Locate every blood parasite and identify its species.
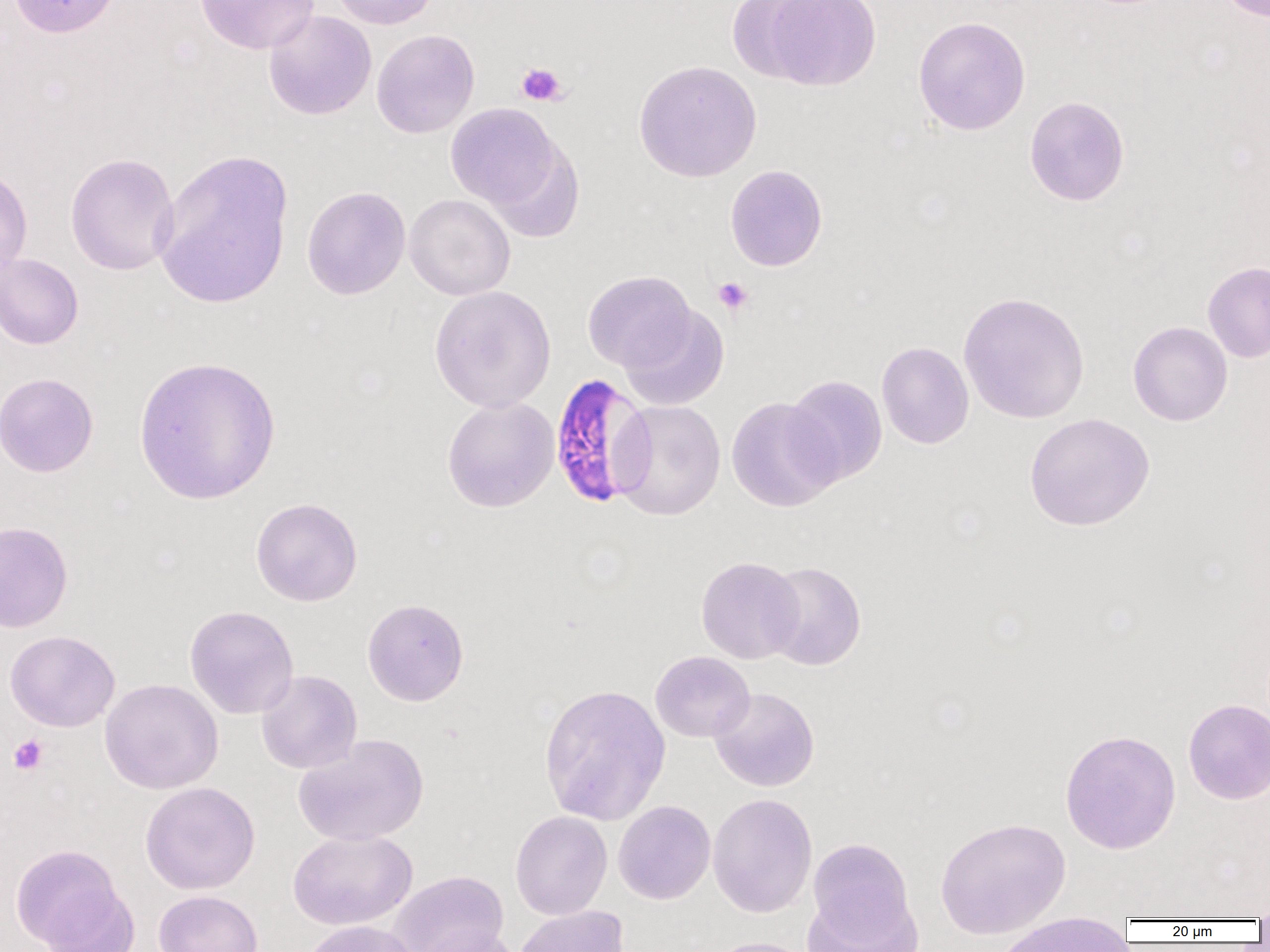

Approximate bounding boxes as (x1,y1)-(x2,y2) corner pairs in pixels.
Plasmodium falciparum-infected red blood cells: (555,372)-(662,507).
No Plasmodium ovale, Plasmodium malariae, Plasmodium vivax, Babesia divergens, or Trypanosoma brucei observed.

slide-level diagnosis = Plasmodium falciparum
platelet locations = approximate bounding boxes as (x1,y1)-(x2,y2) corner pairs in pixels: (516,62)-(567,106), (712,276)-(754,316), (9,735)-(48,774)
modality = light microscopy
field of view = one of a larger specimen
image size = 1270×952 pixels
magnification = 1000x
uninfected red blood cell locations = approximate bounding boxes as (x1,y1)-(x2,y2) corner pairs in pixels: (7,0)-(123,38), (195,0)-(319,54), (329,0)-(440,29), (727,0)-(826,83), (765,0)-(881,91), (1216,0)-(1269,22), (263,10)-(377,120), (913,16)-(1031,135), (371,29)-(480,138), (633,60)-(762,183), (1025,96)-(1129,207), (445,103)-(562,211), (487,139)-(585,243), (151,148)-(294,309), (65,153)-(180,276), (725,164)-(827,271), (0,165)-(33,278), (302,186)-(411,299), (404,193)-(516,301), (0,253)-(83,350), (1202,261)-(1270,363), (582,270)-(696,373), (429,285)-(556,412), (958,291)-(1090,424), (620,304)-(729,411), (1128,321)-(1232,426), (876,341)-(974,449), (133,356)-(281,506), (0,372)-(99,477), (784,374)-(887,486), (441,396)-(560,513), (726,397)-(841,512), (610,400)-(726,521), (1025,412)-(1155,531), (251,497)-(363,607), (0,521)-(73,633), (696,556)-(804,664), (762,561)-(866,671), (362,598)-(469,706), (184,605)-(299,719), (5,630)-(120,732), (650,651)-(755,742), (256,670)-(362,774), (100,678)-(224,794), (538,682)-(671,826), (709,687)-(820,792), (1183,698)-(1270,804), (1059,728)-(1181,855), (292,734)-(429,846), (140,781)-(260,894), (708,792)-(818,918), (613,800)-(716,904), (511,810)-(613,920), (935,816)-(1071,939), (288,829)-(417,931), (807,838)-(918,947), (11,843)-(128,950), (387,871)-(509,952), (36,886)-(140,952), (154,890)-(263,952), (513,905)-(630,952), (994,915)-(1133,952), (300,920)-(422,952), (415,926)-(525,952), (701,936)-(817,952)
preparation = thin blood film